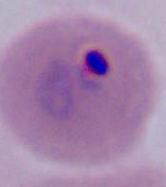 A Plasmodium parasite is seen. Captured at either 400x or 1000x magnification. Micrograph.